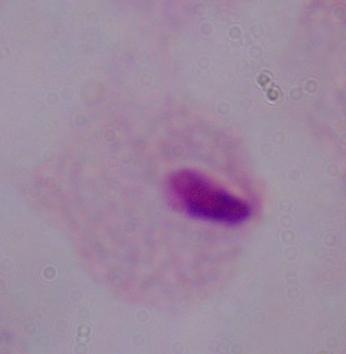 Captured at 1000x magnification. Photomicrograph. A trichomonad is shown.